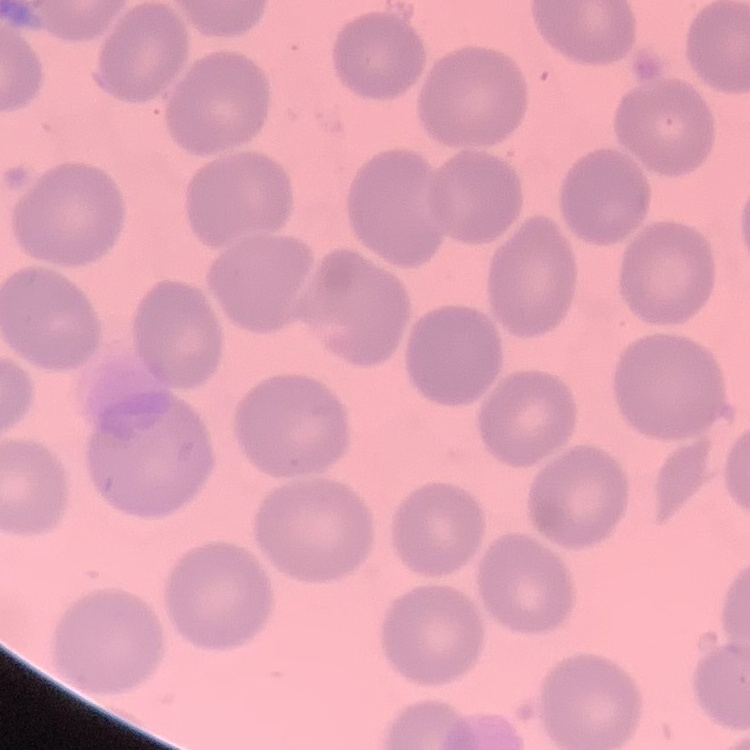

erythrocyte morphology = no rouleaux formation
preparation = thin blood smear
image type = one tile cut from a larger photomicrograph
stain = Field's or Giemsa